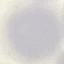
Result: no malaria parasites seen. Acquired by smartphone through the microscope eyepiece. Thin blood film. Cell patch, automatically extracted from a larger field of view and resized to 64 × 64 pixels. Giemsa stain.